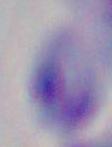
Summary:
  - Identification: Toxoplasma gondii
  - Magnification: 1000x
  - Modality: photomicrograph